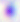
Toxoplasma gondii is shown. Captured at 400x magnification. Photomicrograph.